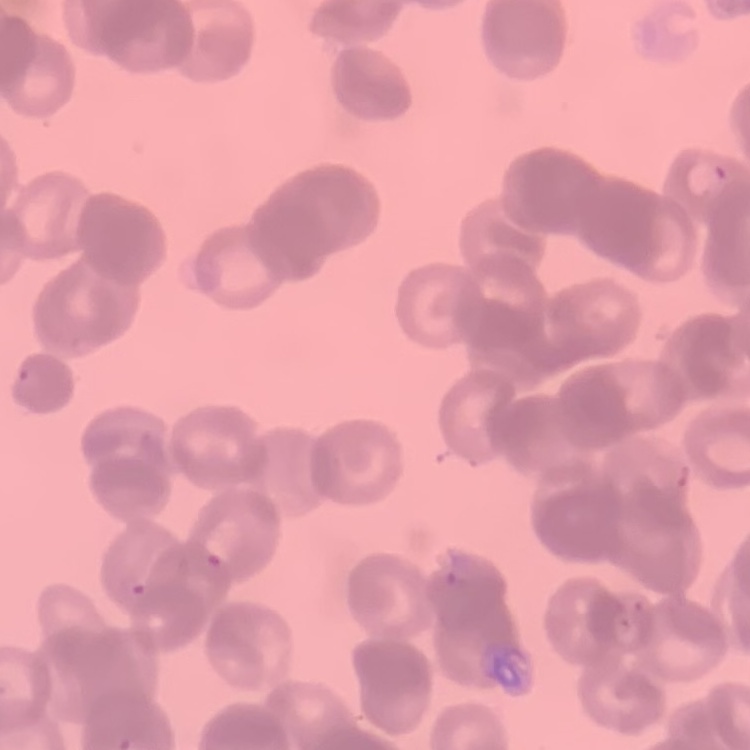
{
  "red_blood_cell_morphology": "rouleaux formation",
  "preparation": "thin blood film",
  "stain": "Field's or Giemsa",
  "image_type": "square crop of a larger photomicrograph"
}